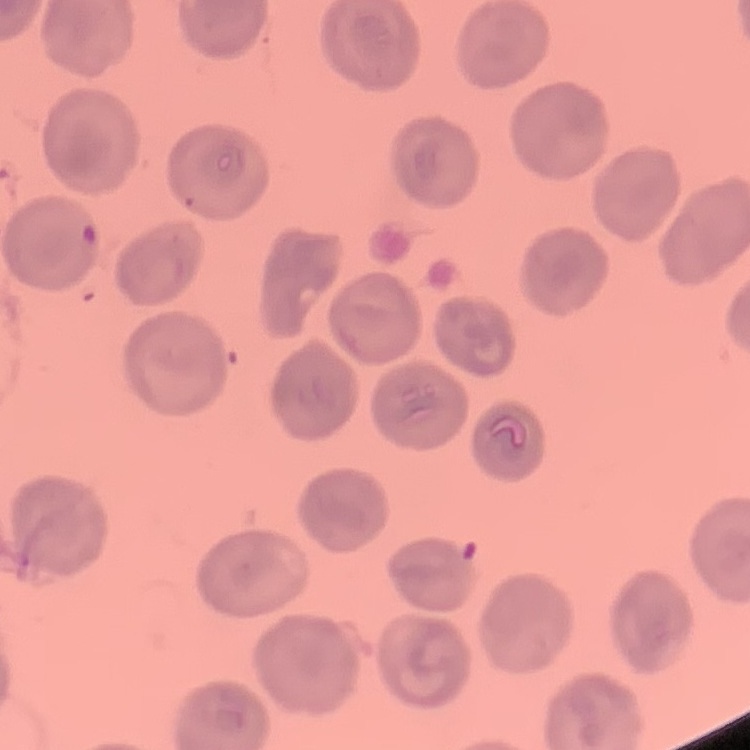
red blood cell morphology = no rouleaux formation
preparation = thin blood film
image type = one tile cut from a larger photomicrograph
stain = Field's or Giemsa